Point out each Plasmodium parasite.
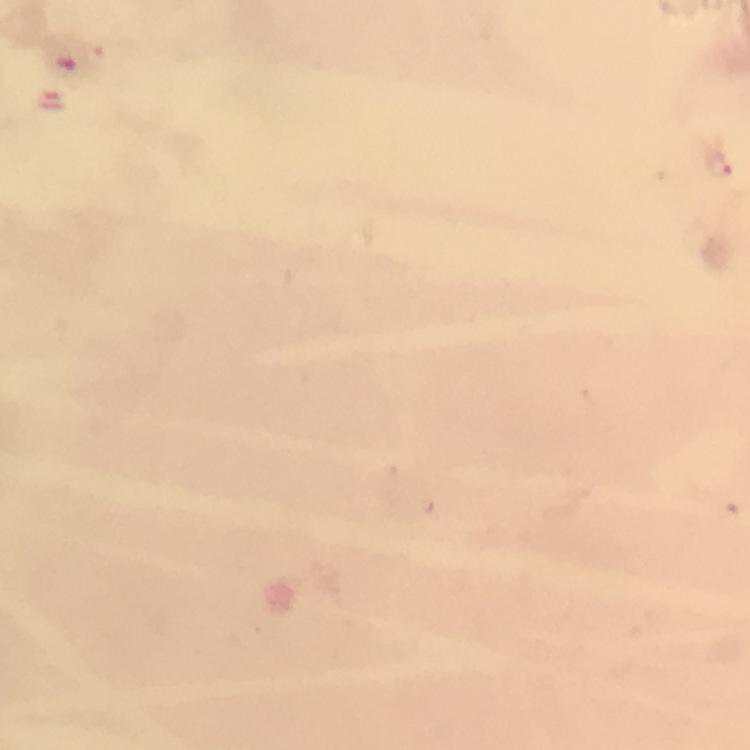

Approximate centers as [x, y] in pixels.
Plasmodium parasites: [719, 166].

From a malaria diagnostic workup. 100x magnification. Immersion oil applied. Image is 750×750 pixels. A crop from one field of view. Smartphone photograph taken through a microscope. Giemsa-stained preparation. Thick blood film.